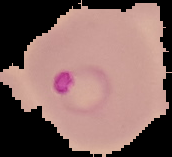

From a thin blood film. Segmented cell region on a black background. Malaria status: parasitized. Image is 172×157 pixels.